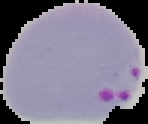

result = Plasmodium parasites identified
image type = segmented cell region with the area outside set to black
image size = 148×124 pixels
preparation = thin blood smear